Point out every Plasmodium parasite.
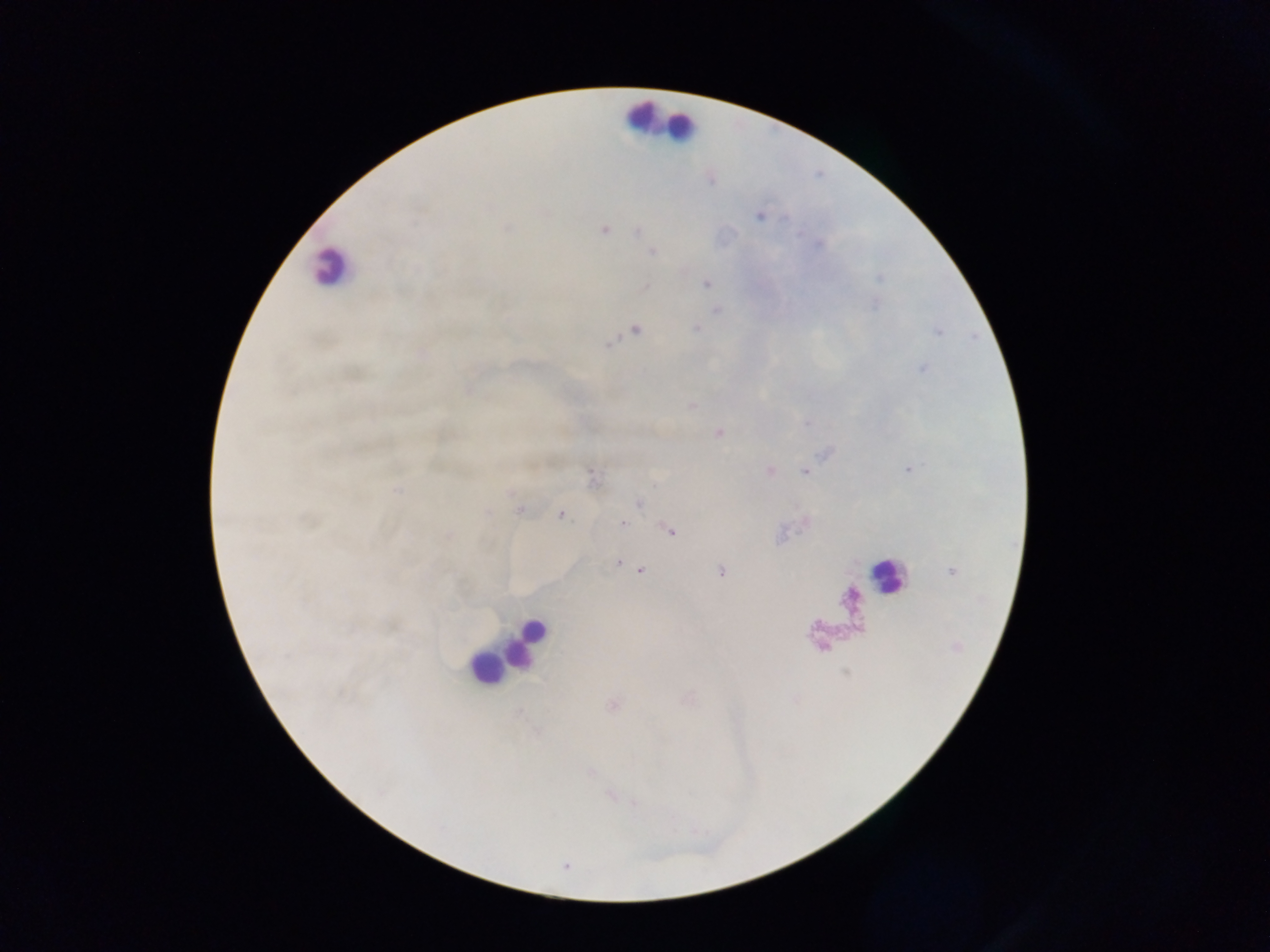
Approximate centers as x y in pixels.
Plasmodium parasites: 709 179; 759 216; 604 230; 639 231; 652 251; 707 284; 645 286; 717 309; 695 328; 634 329; 607 343; 922 368; 468 390; 692 405; 718 432; 909 469; 769 470; 805 471; 591 476; 638 503; 520 510; 561 514; 308 519; 805 522; 622 523; 670 531; 447 536; 618 562; 625 564; 640 570; 951 571; 720 572; 613 704; 590 772; 611 794; 566 866.

image_size: 1270×952 pixels
capture: mobile-phone photograph through a microscope
preparation: thick blood film
leukocyte_locations: 'approximate centers as x y in pixels: 639 116; 657 120; 680 126; 330 267; 888 577; 531 630; 518 645; 503 660; 487 669'
field_of_view: single
country: Ghana